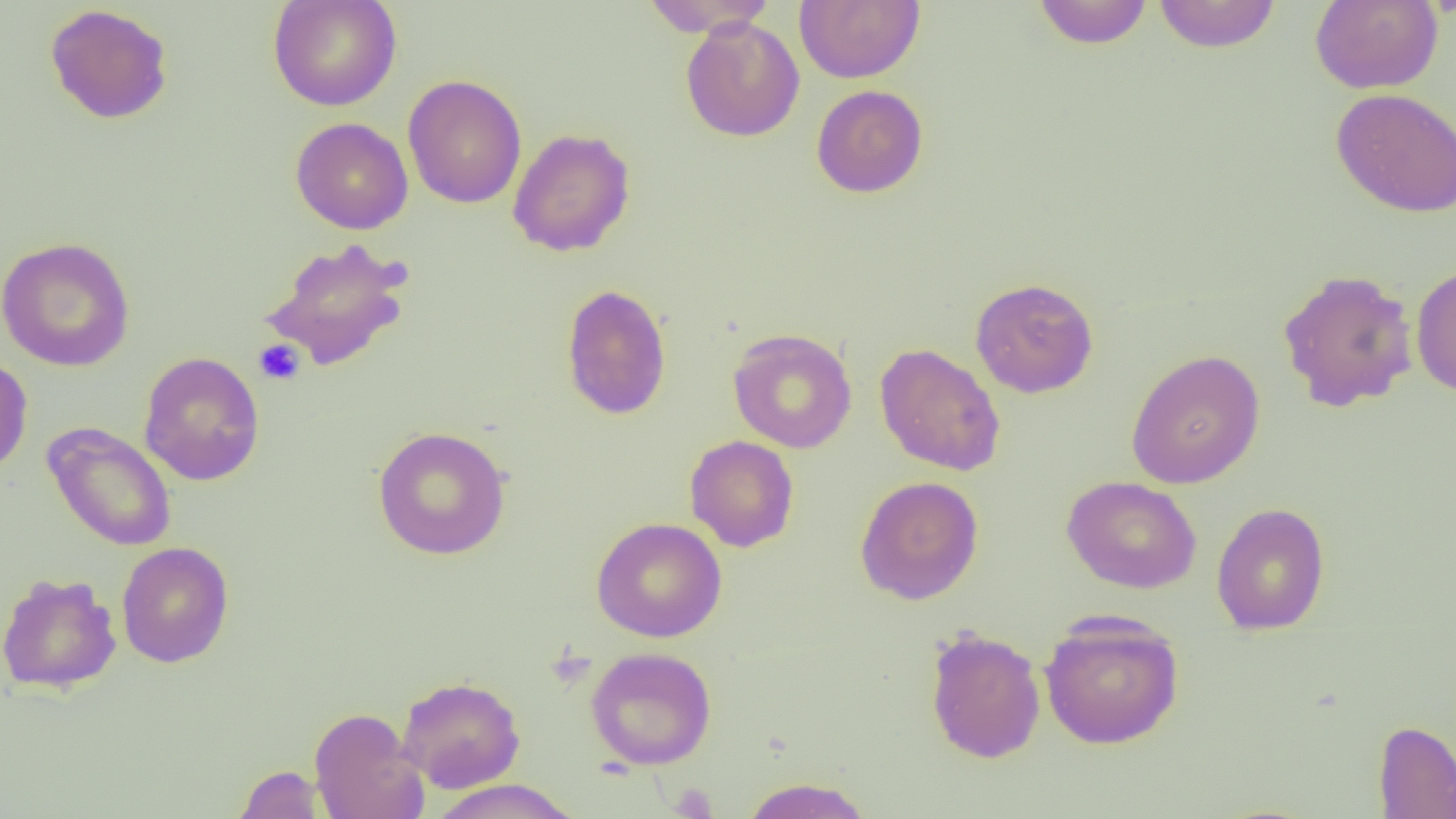

Summary:
  - Coordinate format: approximate bounding boxes as [x1, y1, x2, y2] in pixels
  - Platelet locations: [253, 339, 306, 386], [668, 782, 718, 818]
  - Uninfected red blood cell locations: [267, 0, 402, 112], [640, 0, 777, 37], [794, 0, 924, 84], [1153, 0, 1281, 52], [1309, 0, 1444, 94], [1032, 1, 1154, 49], [44, 4, 174, 124], [680, 16, 805, 142], [403, 74, 527, 209], [811, 84, 928, 198], [1331, 88, 1456, 218], [290, 117, 413, 234], [507, 127, 636, 257], [0, 236, 135, 372], [262, 237, 414, 371], [1411, 263, 1456, 397], [1276, 268, 1419, 412], [970, 277, 1099, 398], [560, 283, 672, 420], [727, 328, 857, 453], [875, 342, 1006, 476], [1125, 349, 1265, 489], [138, 351, 265, 486], [0, 355, 33, 477], [42, 421, 177, 552], [372, 426, 511, 560], [684, 435, 799, 552], [855, 475, 984, 605], [1062, 475, 1202, 594], [1211, 502, 1330, 635], [591, 517, 727, 642], [116, 541, 234, 668], [0, 572, 122, 694], [1039, 613, 1184, 749], [924, 627, 1046, 764], [586, 646, 717, 770], [397, 675, 526, 792], [309, 707, 428, 819], [1373, 719, 1456, 818], [233, 764, 325, 819], [740, 776, 873, 819], [428, 778, 582, 819]
  - Slide-level diagnosis: no evidence of blood parasites
  - Magnification: 1000x
  - Field of view: one of a larger specimen
  - Image size: 1456×819 pixels
  - Modality: light microscopy
  - Preparation: thin blood smear